Outline each blood parasite and name the species.
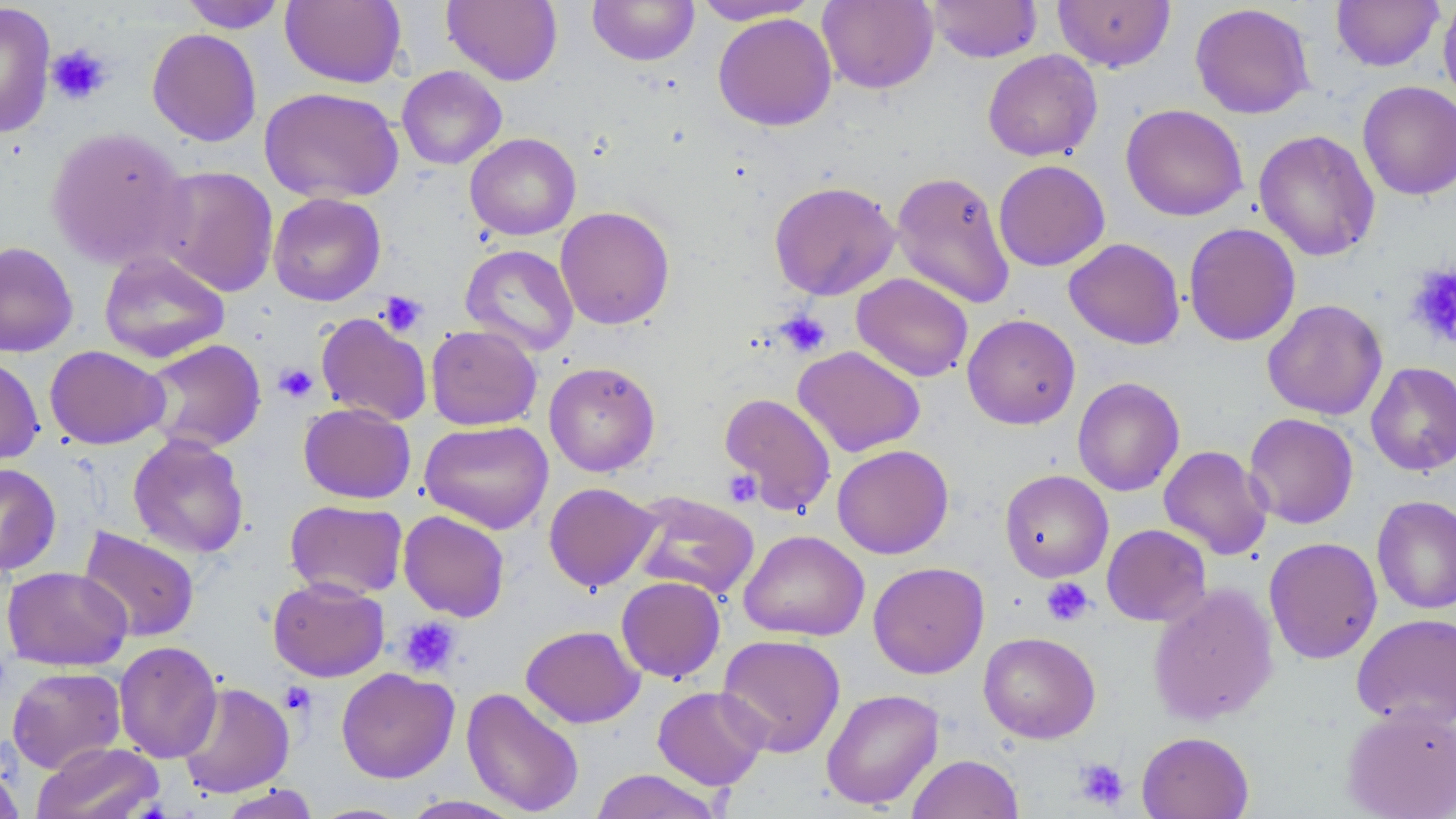

No blood parasites observed.

Approximate bounding boxes as [x1, y1, x2, y2] in pixels. Uninfected red blood cell locations (subset): [179, 0, 288, 33], [280, 0, 406, 88], [442, 0, 563, 86], [587, 0, 700, 66], [692, 0, 819, 25], [817, 0, 938, 94], [927, 0, 1042, 63], [1331, 0, 1444, 72], [1438, 0, 1456, 109], [1053, 1, 1175, 72], [0, 2, 56, 139], [1190, 3, 1315, 119], [713, 13, 837, 131], [147, 28, 262, 147], [982, 49, 1103, 162], [397, 66, 507, 170], [1357, 81, 1456, 200], [260, 87, 404, 204], [1121, 103, 1248, 222], [45, 125, 190, 269], [1254, 129, 1380, 261], [465, 133, 581, 240], [993, 160, 1110, 271], [153, 165, 280, 297], [891, 170, 1015, 309], [769, 180, 901, 301], [268, 193, 386, 306], [554, 206, 675, 329], [1183, 222, 1301, 346], [1064, 238, 1185, 349], [0, 241, 78, 357], [460, 244, 579, 356], [99, 251, 230, 363], [851, 273, 974, 382], [1262, 299, 1387, 420], [315, 312, 433, 426], [962, 313, 1081, 429], [425, 324, 542, 431], [141, 339, 267, 453], [45, 345, 169, 449], [792, 345, 925, 458], [0, 356, 44, 466], [544, 361, 661, 477], [1365, 362, 1456, 476], [1072, 376, 1185, 496], [298, 402, 416, 504], [1244, 413, 1358, 529], [419, 420, 554, 534], [128, 434, 250, 559], [832, 444, 954, 559], [1159, 445, 1272, 560], [0, 462, 61, 576], [999, 469, 1113, 581], [543, 482, 660, 592], [628, 491, 760, 600], [1371, 495, 1456, 615], [284, 499, 408, 600], [398, 510, 510, 622], [1101, 524, 1211, 626], [77, 527, 200, 643], [738, 529, 869, 641], [1263, 536, 1382, 664], [868, 561, 990, 678], [2, 566, 133, 671], [616, 576, 726, 683], [268, 577, 390, 682], [1148, 583, 1279, 726], [1351, 613, 1456, 730], [520, 625, 644, 728], [978, 631, 1101, 743], [716, 633, 846, 757], [113, 641, 222, 763], [7, 666, 126, 773], [336, 667, 459, 783], [177, 681, 294, 798], [652, 685, 771, 790], [461, 687, 584, 816], [821, 688, 944, 810], [1342, 705, 1456, 819], [1136, 731, 1254, 819], [32, 742, 163, 819], [906, 753, 1025, 819], [0, 762, 25, 819], [589, 769, 724, 819], [217, 784, 320, 818], [398, 795, 527, 818], [306, 802, 416, 818]. Platelet locations (subset): [46, 44, 112, 106], [1406, 263, 1456, 347], [377, 291, 428, 337], [774, 310, 831, 358], [274, 363, 318, 403], [722, 469, 761, 507], [1042, 577, 1094, 626], [397, 616, 461, 677], [280, 681, 316, 716], [1073, 758, 1129, 810]. Slide-level diagnosis: negative for blood parasites. 1000x magnification. One field of a larger specimen. Image is 1456×819 pixels. Optical microscopy. Thin blood smear. May-Grünwald-Giemsa-stained preparation.